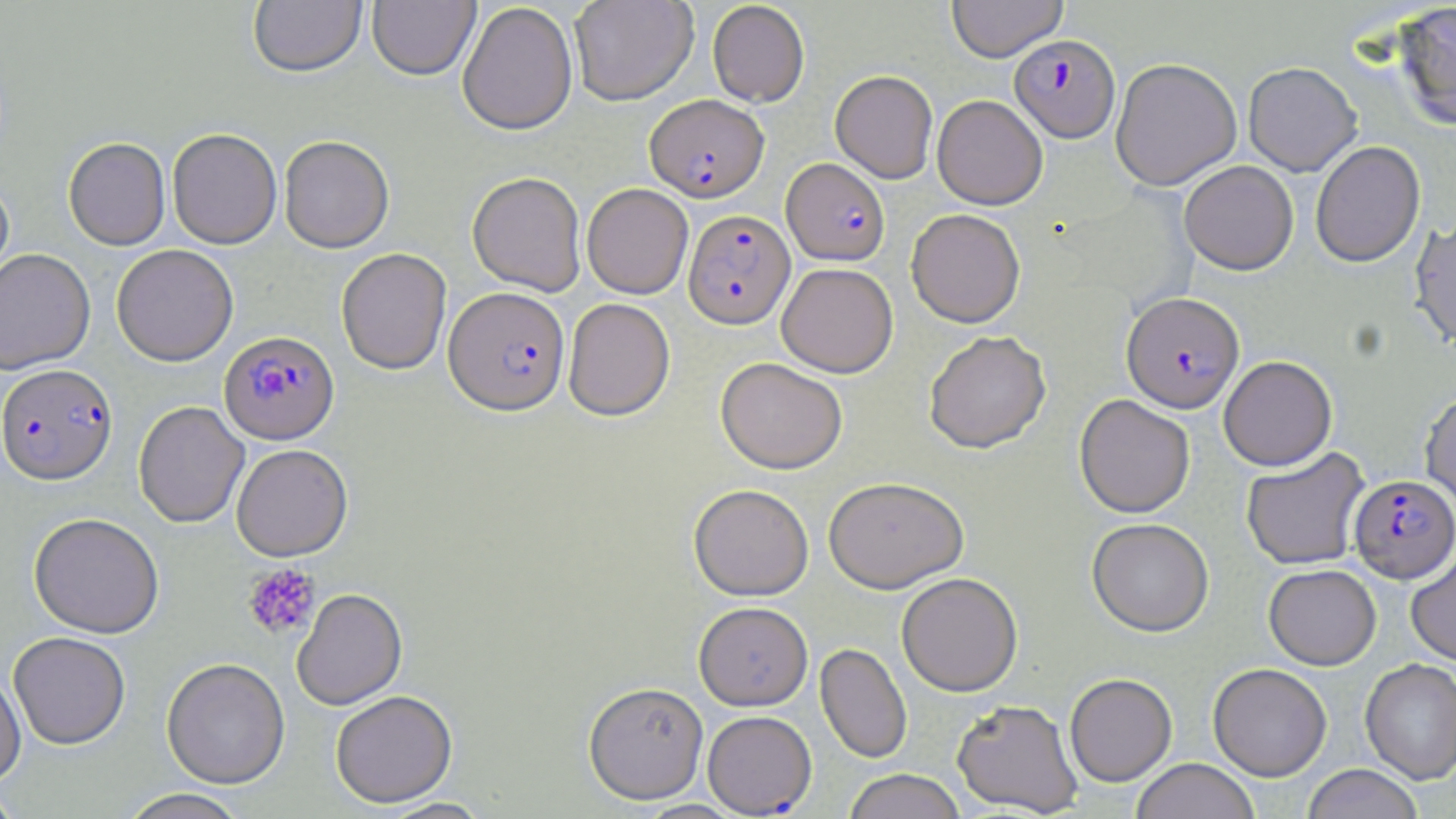
slide-level diagnosis = Plasmodium falciparum
preparation = thin blood smear
stain = May-Grünwald-Giemsa
modality = optical microscopy
image size = 1456×819 pixels
field of view = single
magnification = 1000x
uninfected red blood cell locations = approximate bounding boxes as [x1, y1, x2, y2] in pixels: [367, 0, 480, 81], [569, 0, 698, 105], [946, 0, 1067, 62], [248, 1, 367, 78], [707, 1, 810, 107], [1391, 1, 1456, 131], [457, 2, 578, 136], [1110, 57, 1242, 190], [1243, 61, 1362, 176], [830, 70, 938, 183], [932, 94, 1048, 210], [167, 128, 282, 249], [279, 135, 394, 252], [63, 137, 170, 250], [1310, 140, 1425, 267], [1179, 160, 1299, 275], [467, 171, 587, 296], [0, 177, 14, 294], [582, 183, 693, 299], [906, 208, 1025, 327], [1410, 216, 1456, 352], [112, 244, 238, 366], [0, 248, 95, 374], [336, 248, 452, 375], [776, 262, 898, 377], [563, 298, 675, 421], [924, 330, 1051, 453], [1218, 355, 1337, 471], [715, 357, 848, 474], [1420, 389, 1456, 514], [1074, 394, 1195, 518], [134, 401, 249, 528], [231, 444, 353, 561], [1241, 447, 1370, 570], [823, 475, 969, 592], [689, 484, 814, 600], [29, 513, 165, 638], [1087, 518, 1214, 636], [1406, 549, 1456, 666], [1263, 563, 1381, 669], [896, 572, 1022, 696], [292, 588, 408, 710], [694, 601, 813, 711], [9, 632, 130, 750], [815, 643, 912, 764], [161, 657, 290, 789], [1360, 658, 1456, 784], [1208, 663, 1332, 781], [0, 669, 26, 787], [1064, 673, 1177, 786], [583, 681, 709, 804], [331, 690, 458, 807], [952, 698, 1083, 816], [702, 710, 817, 816], [1130, 758, 1260, 819], [1303, 764, 1423, 819], [842, 769, 967, 819], [0, 784, 25, 818], [117, 788, 251, 819], [377, 798, 495, 819], [634, 799, 747, 818]
platelet locations = approximate bounding boxes as [x1, y1, x2, y2] in pixels: [242, 563, 320, 640]
Plasmodium falciparum-infected red blood cell locations = approximate bounding boxes as [x1, y1, x2, y2] in pixels: [1009, 34, 1120, 143], [645, 94, 768, 202], [782, 157, 889, 266], [684, 209, 795, 328], [444, 286, 570, 415], [1122, 292, 1244, 413], [219, 330, 339, 444], [0, 364, 118, 485], [1349, 474, 1455, 583]